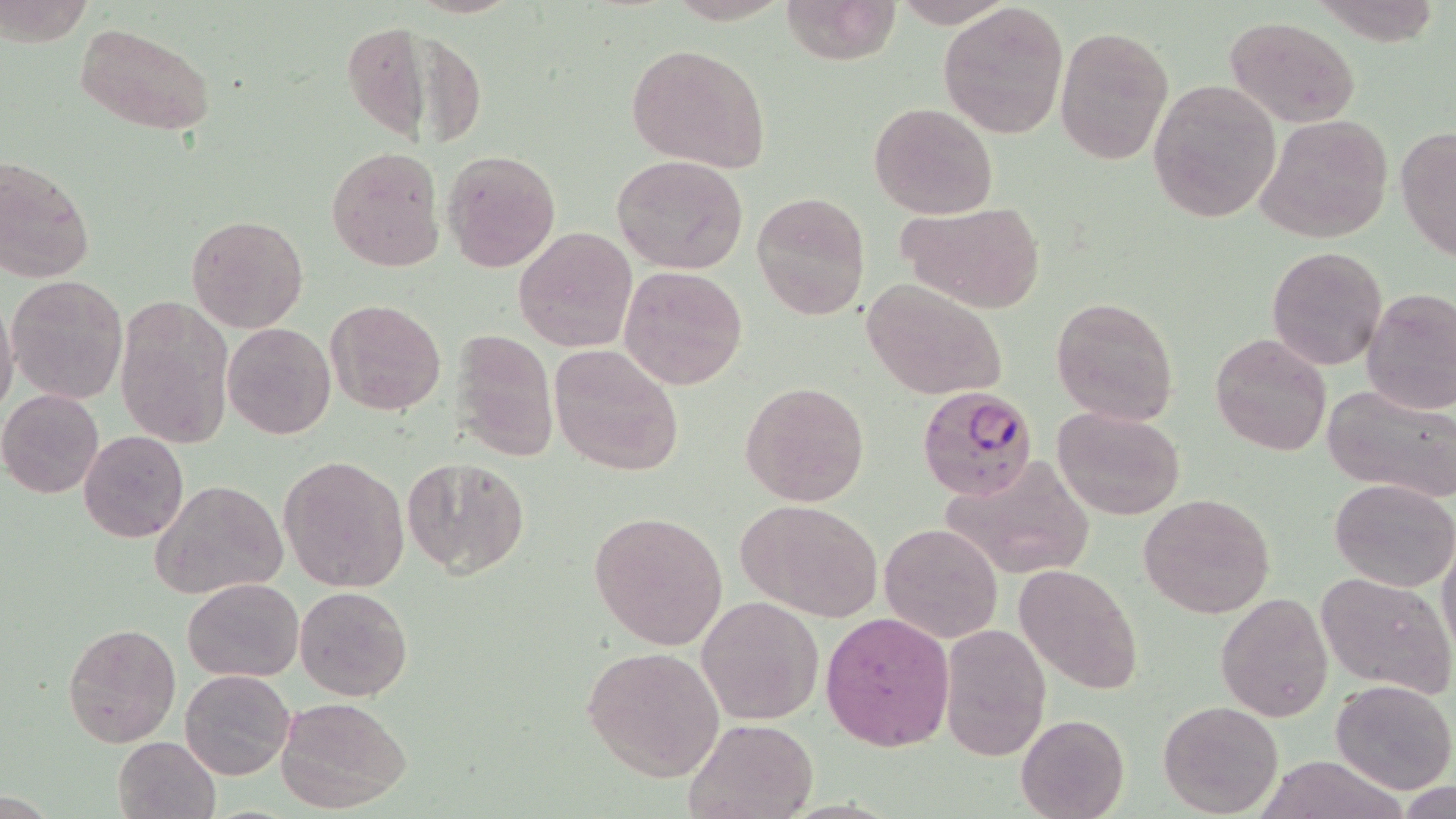
Summary:
  - Coordinate format: approximate bounding boxes as (x1, y1, x2, y2) in pixels
  - Uninfected red blood cell locations: (779, 0, 902, 66), (939, 2, 1071, 141), (1226, 16, 1359, 127), (343, 21, 432, 142), (75, 23, 218, 137), (1054, 26, 1173, 165), (625, 43, 772, 172), (1148, 77, 1280, 223), (868, 102, 999, 219), (1254, 113, 1394, 246), (1395, 126, 1456, 263), (326, 145, 445, 272), (443, 148, 561, 274), (611, 154, 749, 274), (0, 156, 95, 282), (752, 191, 870, 320), (898, 202, 1046, 313), (186, 214, 309, 331), (514, 227, 636, 351), (1267, 246, 1386, 371), (619, 266, 748, 389), (6, 275, 129, 405), (863, 278, 1009, 401), (1361, 286, 1456, 415), (115, 295, 233, 451), (1051, 295, 1180, 426), (0, 296, 19, 420), (326, 299, 447, 416), (223, 323, 335, 439), (450, 327, 559, 463), (1209, 331, 1331, 457), (549, 344, 686, 477), (739, 379, 870, 508), (1323, 381, 1456, 503), (0, 390, 104, 498), (1053, 405, 1185, 520), (80, 430, 189, 544), (279, 454, 409, 593), (402, 455, 529, 578), (938, 458, 1095, 582), (1328, 476, 1456, 590), (149, 480, 287, 600), (1138, 491, 1277, 620), (737, 500, 884, 622), (589, 510, 729, 651), (881, 523, 1001, 643), (1438, 535, 1456, 658), (1015, 563, 1143, 695), (1315, 570, 1456, 698), (182, 578, 304, 681), (294, 584, 414, 701), (1216, 590, 1333, 722), (696, 596, 823, 724), (821, 611, 953, 751), (62, 622, 180, 747), (938, 622, 1049, 759), (582, 646, 725, 781), (180, 668, 296, 780), (1330, 678, 1456, 793), (277, 697, 410, 812), (1157, 699, 1283, 816), (1015, 714, 1129, 819), (684, 717, 819, 818), (112, 735, 220, 819)
  - Plasmodium falciparum-infected red blood cell locations: (916, 384, 1041, 501)
  - Slide-level diagnosis: Plasmodium falciparum
  - Field of view: one of a larger specimen
  - Image size: 1456×819 pixels
  - Modality: optical microscopy
  - Magnification: 1000x
  - Stain: May-Grünwald-Giemsa
  - Preparation: thin blood smear